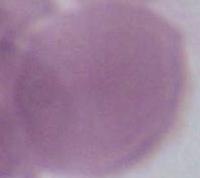

An erythrocyte is seen. Photomicrograph. Captured at 1000x magnification.